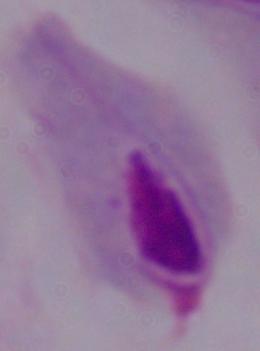 A trichomonad is seen. 1000x magnification. Photomicrograph.